Give the position of every P. falciparum parasite, noting its life-cycle stage.
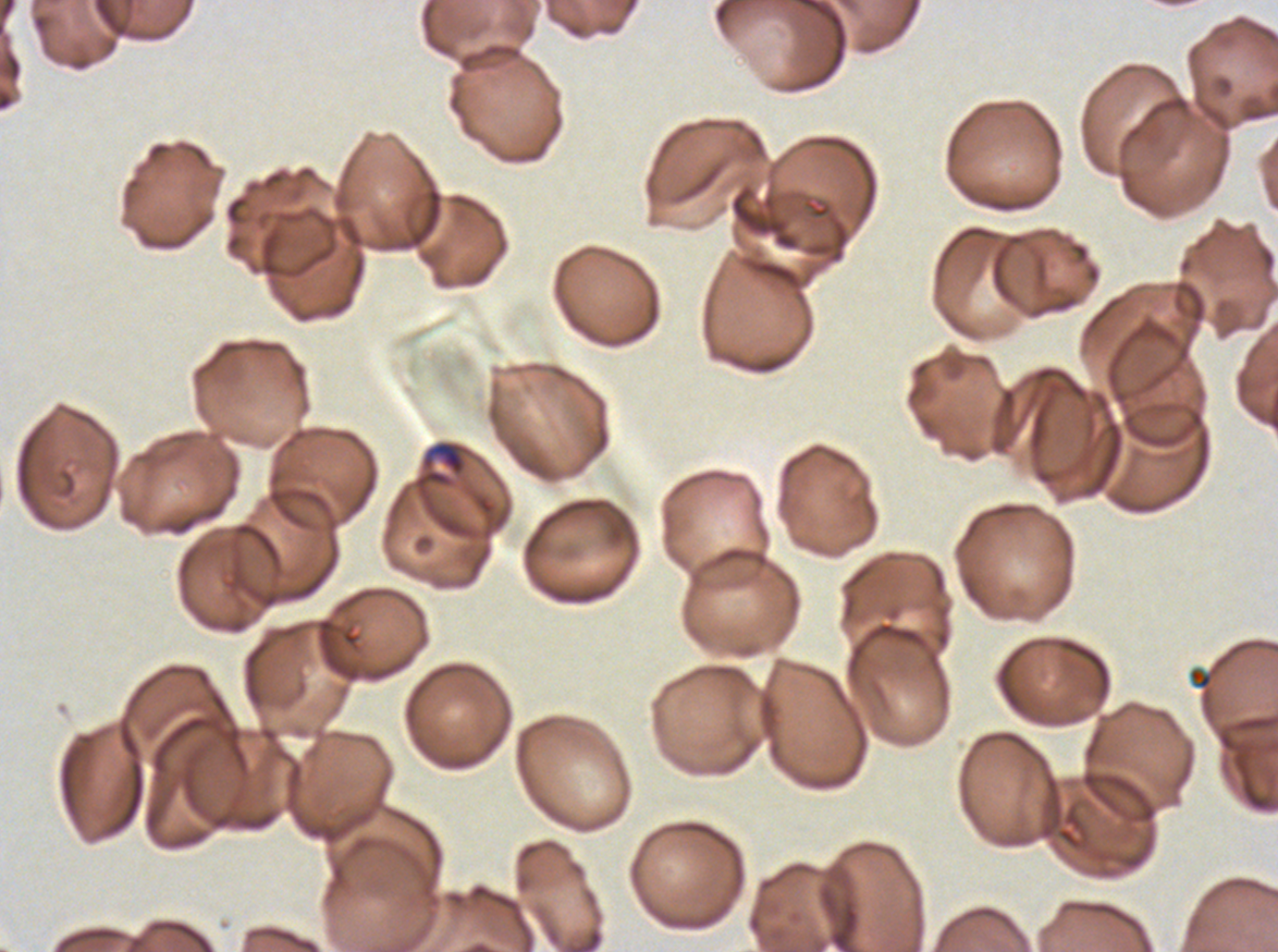

Approximate bounding boxes as (x1, y1, x2, y2) in pixels.
Mid trophozoites: (421, 440, 466, 476).
No rings, late-ring/early-trophozoite forms, late trophozoites, early schizonts, late schizonts, segmenters, or gametocytes observed.

{
  "image_size": "1278×952 pixels",
  "preparation": "thin blood film",
  "stain": "Giemsa",
  "debris_locations": "approximate bounding boxes as (x1, y1, x2, y2) in pixels: (1188, 667, 1212, 690)",
  "specimen": "P. falciparum from a patient in The Gambia, cultured ex vivo for 24 to 48 hours",
  "field_of_view": "sub-image separated from a larger composite"
}